Point out each leukocyte.
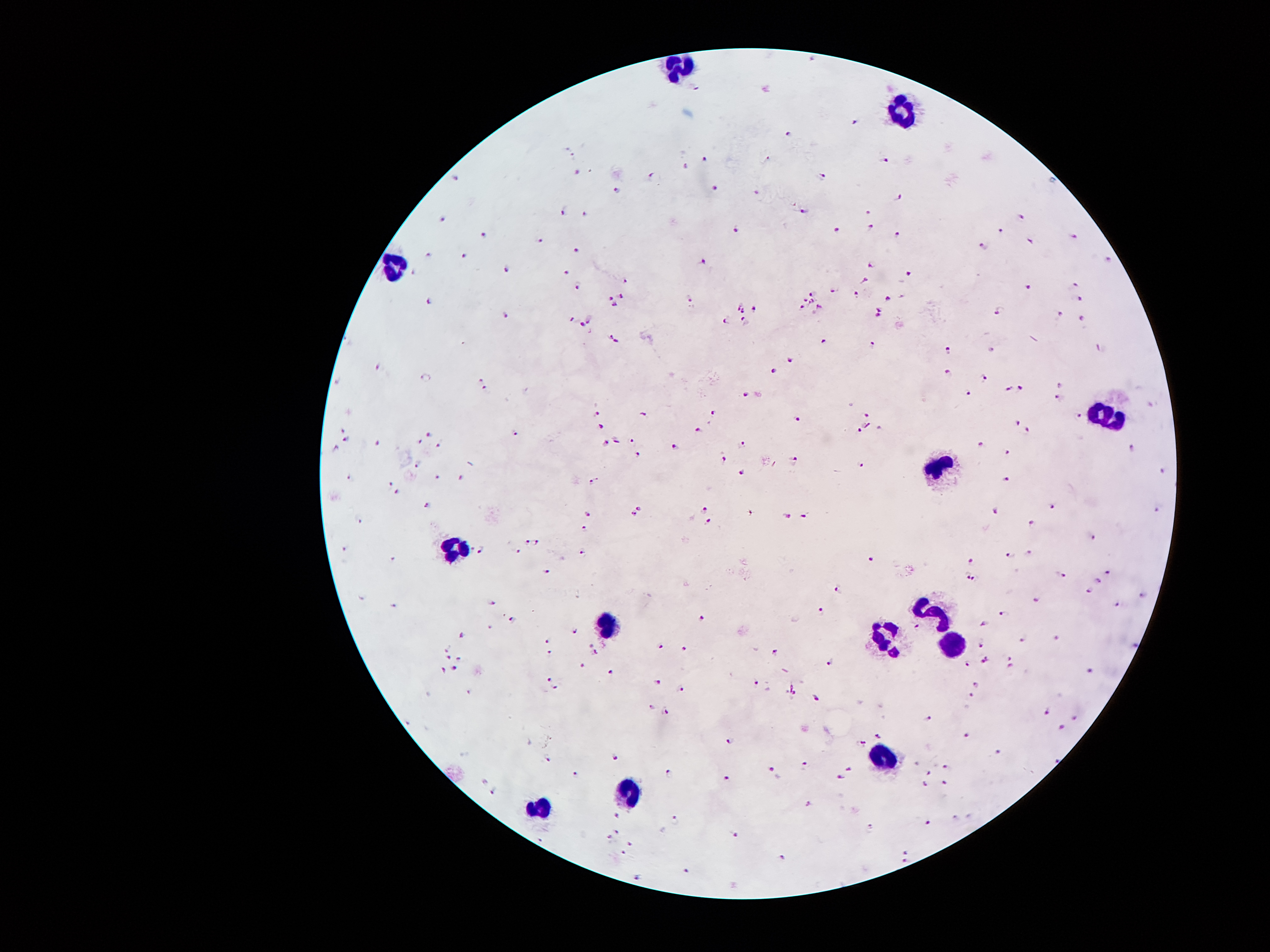

Approximate object centers, in pixels from the top-left corner.
Leukocytes: (x=680, y=67), (x=902, y=110), (x=394, y=267), (x=1106, y=416), (x=939, y=471), (x=455, y=547), (x=935, y=615), (x=605, y=627), (x=882, y=636), (x=951, y=645), (x=885, y=757), (x=628, y=791), (x=540, y=805).

malaria parasite locations = (x=697, y=87), (x=857, y=123), (x=788, y=136), (x=573, y=156), (x=703, y=160), (x=884, y=160), (x=578, y=174), (x=653, y=177), (x=822, y=177), (x=457, y=179), (x=715, y=188), (x=615, y=191), (x=756, y=194), (x=897, y=197), (x=804, y=211), (x=562, y=212), (x=868, y=213), (x=584, y=215), (x=441, y=218), (x=1022, y=218), (x=736, y=229), (x=870, y=229), (x=1000, y=230), (x=838, y=232), (x=486, y=235), (x=896, y=235), (x=1074, y=236), (x=540, y=240), (x=1030, y=240), (x=984, y=247), (x=576, y=251), (x=429, y=255), (x=463, y=257), (x=1108, y=260), (x=703, y=262), (x=872, y=265), (x=505, y=269), (x=413, y=274), (x=908, y=274), (x=567, y=275), (x=626, y=282), (x=865, y=282), (x=1076, y=284), (x=576, y=286), (x=1029, y=287), (x=834, y=289), (x=812, y=294), (x=858, y=294), (x=621, y=296), (x=610, y=298), (x=688, y=298), (x=888, y=298), (x=1082, y=299), (x=805, y=300), (x=812, y=301), (x=425, y=302), (x=614, y=305), (x=738, y=306), (x=820, y=306), (x=802, y=308), (x=755, y=309), (x=879, y=309), (x=999, y=310), (x=742, y=312), (x=505, y=315), (x=1060, y=315), (x=877, y=317), (x=727, y=318), (x=572, y=319), (x=589, y=319), (x=1082, y=319), (x=744, y=320), (x=580, y=325), (x=614, y=340), (x=824, y=342), (x=874, y=343), (x=1100, y=349), (x=949, y=350), (x=790, y=359), (x=376, y=366), (x=774, y=371), (x=950, y=374), (x=481, y=379), (x=985, y=379), (x=1061, y=386), (x=1021, y=389), (x=1009, y=391), (x=487, y=392), (x=747, y=393), (x=968, y=393), (x=1058, y=398), (x=595, y=415), (x=643, y=415), (x=715, y=415), (x=869, y=416), (x=1080, y=417), (x=798, y=419), (x=1017, y=423), (x=602, y=427), (x=343, y=429), (x=698, y=430), (x=1027, y=430), (x=861, y=431), (x=426, y=433), (x=514, y=434), (x=348, y=439), (x=605, y=441), (x=632, y=441), (x=420, y=442), (x=377, y=444), (x=742, y=444), (x=439, y=445), (x=981, y=445), (x=674, y=448), (x=1130, y=448), (x=334, y=449), (x=1008, y=453), (x=636, y=456), (x=724, y=459), (x=795, y=460), (x=418, y=464), (x=861, y=465), (x=743, y=471), (x=1162, y=472), (x=438, y=476), (x=348, y=477), (x=1009, y=479), (x=461, y=480), (x=593, y=482), (x=390, y=484), (x=395, y=492), (x=427, y=505), (x=642, y=505), (x=1050, y=508), (x=703, y=509), (x=1157, y=509), (x=994, y=511), (x=590, y=514), (x=632, y=516), (x=784, y=516), (x=803, y=517), (x=360, y=519), (x=707, y=523), (x=1033, y=523), (x=586, y=529), (x=1092, y=537), (x=526, y=542), (x=537, y=543), (x=343, y=547), (x=481, y=549), (x=518, y=550), (x=583, y=554), (x=1030, y=554), (x=1011, y=557), (x=392, y=558), (x=871, y=560), (x=973, y=561), (x=1063, y=571), (x=547, y=572), (x=1106, y=572), (x=965, y=577), (x=975, y=581), (x=1096, y=581), (x=836, y=587), (x=1089, y=590), (x=1144, y=596), (x=1036, y=599), (x=494, y=602), (x=1119, y=604), (x=391, y=606), (x=821, y=607), (x=1004, y=613), (x=701, y=619), (x=514, y=620), (x=981, y=623), (x=918, y=628), (x=574, y=632), (x=463, y=636), (x=1056, y=639), (x=1023, y=641), (x=550, y=642), (x=589, y=644), (x=980, y=644), (x=1135, y=645), (x=660, y=646), (x=446, y=647), (x=685, y=649), (x=596, y=653), (x=550, y=655), (x=774, y=655), (x=1011, y=656), (x=447, y=657), (x=459, y=660), (x=831, y=660), (x=984, y=660), (x=964, y=662), (x=584, y=665), (x=1009, y=668), (x=456, y=669), (x=443, y=670), (x=612, y=672), (x=1092, y=672), (x=549, y=678), (x=657, y=681), (x=755, y=683), (x=978, y=685), (x=556, y=688), (x=680, y=689), (x=791, y=695), (x=971, y=696), (x=816, y=697), (x=652, y=709), (x=1046, y=712), (x=667, y=713), (x=1074, y=718), (x=926, y=719), (x=1060, y=729), (x=877, y=735), (x=968, y=735), (x=731, y=741), (x=861, y=743), (x=998, y=752), (x=614, y=756), (x=548, y=758), (x=945, y=765), (x=804, y=766), (x=850, y=767), (x=774, y=773), (x=928, y=773), (x=576, y=775), (x=668, y=775), (x=839, y=779), (x=725, y=780), (x=482, y=783), (x=944, y=784), (x=925, y=785), (x=494, y=792), (x=809, y=806), (x=615, y=816), (x=675, y=820), (x=929, y=822), (x=872, y=828), (x=617, y=832), (x=732, y=835), (x=608, y=836), (x=630, y=845), (x=904, y=852), (x=623, y=854), (x=781, y=859), (x=903, y=863), (x=687, y=872), (x=637, y=877)
magnification = 100x
field of view = single
patient malaria status = positive for Plasmodium falciparum
preparation = thick blood smear
image size = 1270×952 pixels
capture = smartphone camera through the microscope eyepiece
stain = Giemsa